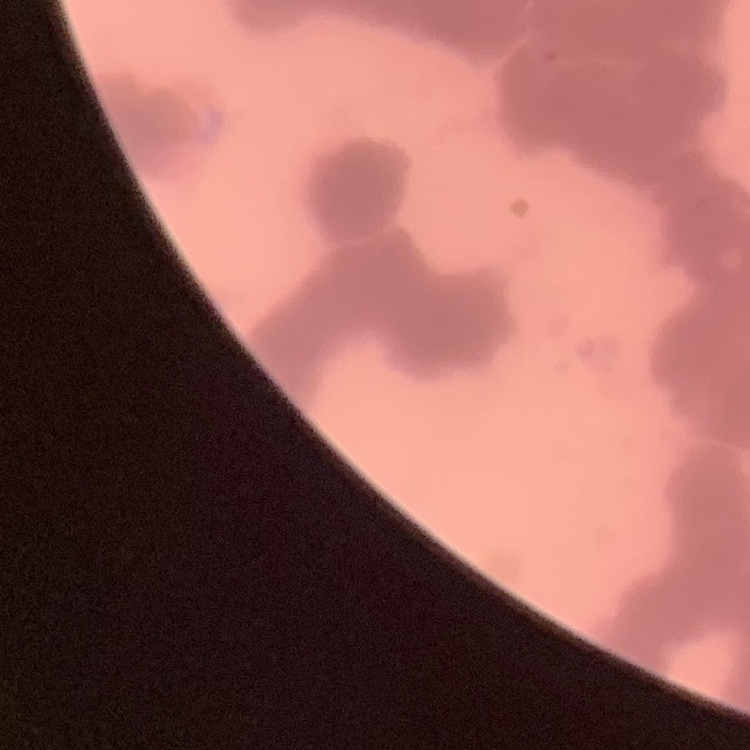

Summary:
  - Erythrocyte morphology: rouleaux formation
  - Image type: square crop of a larger photomicrograph
  - Preparation: thin blood smear
  - Stain: Field's or Giemsa